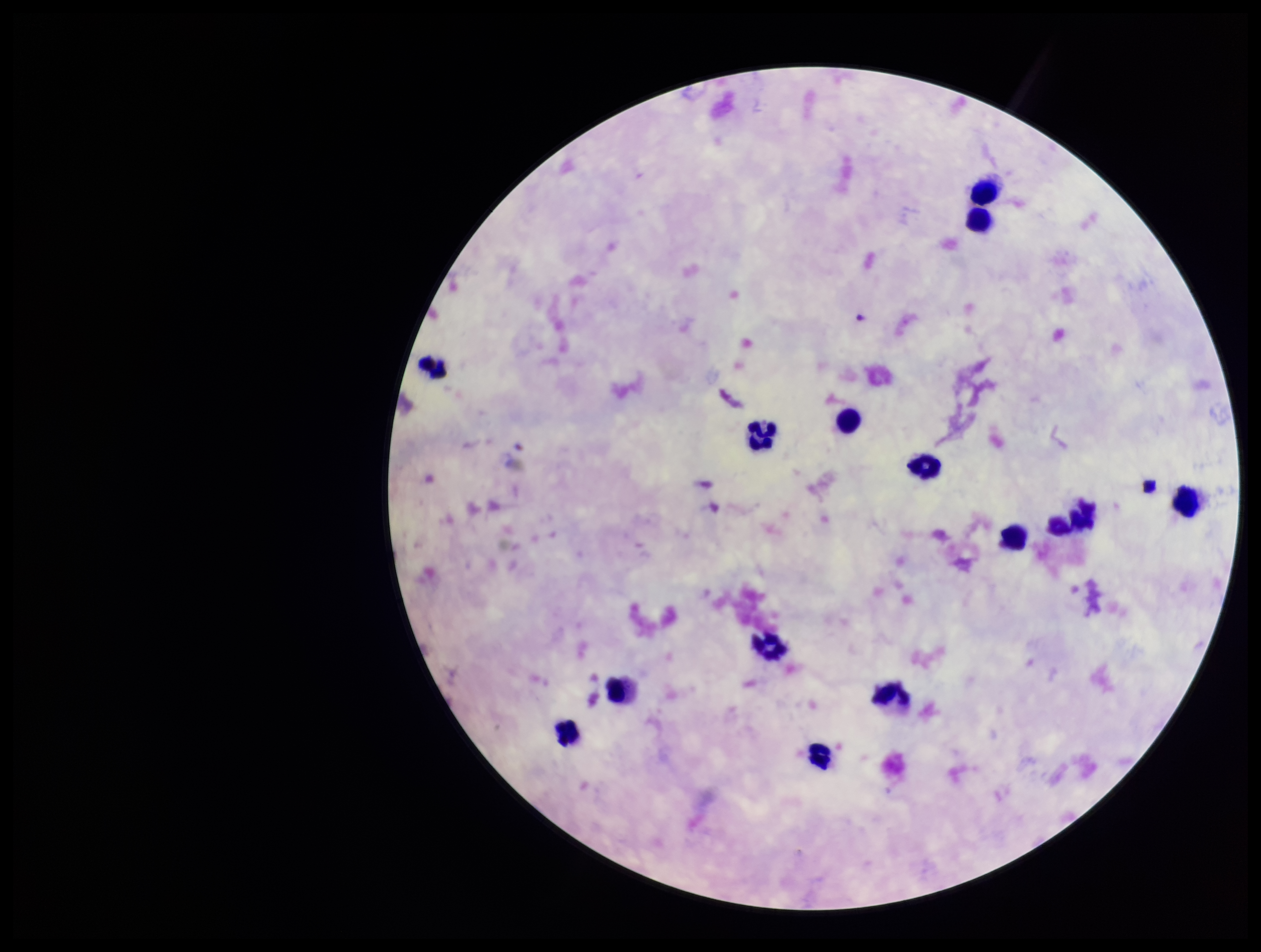

patient malaria status = negative
preparation = thick blood smear
capture = smartphone photograph through the microscope eyepiece
leukocyte count = 14
image size = 1261×952 pixels
field of view = single
parasite count = 0
stain = Giemsa
Plasmodium parasites = none seen